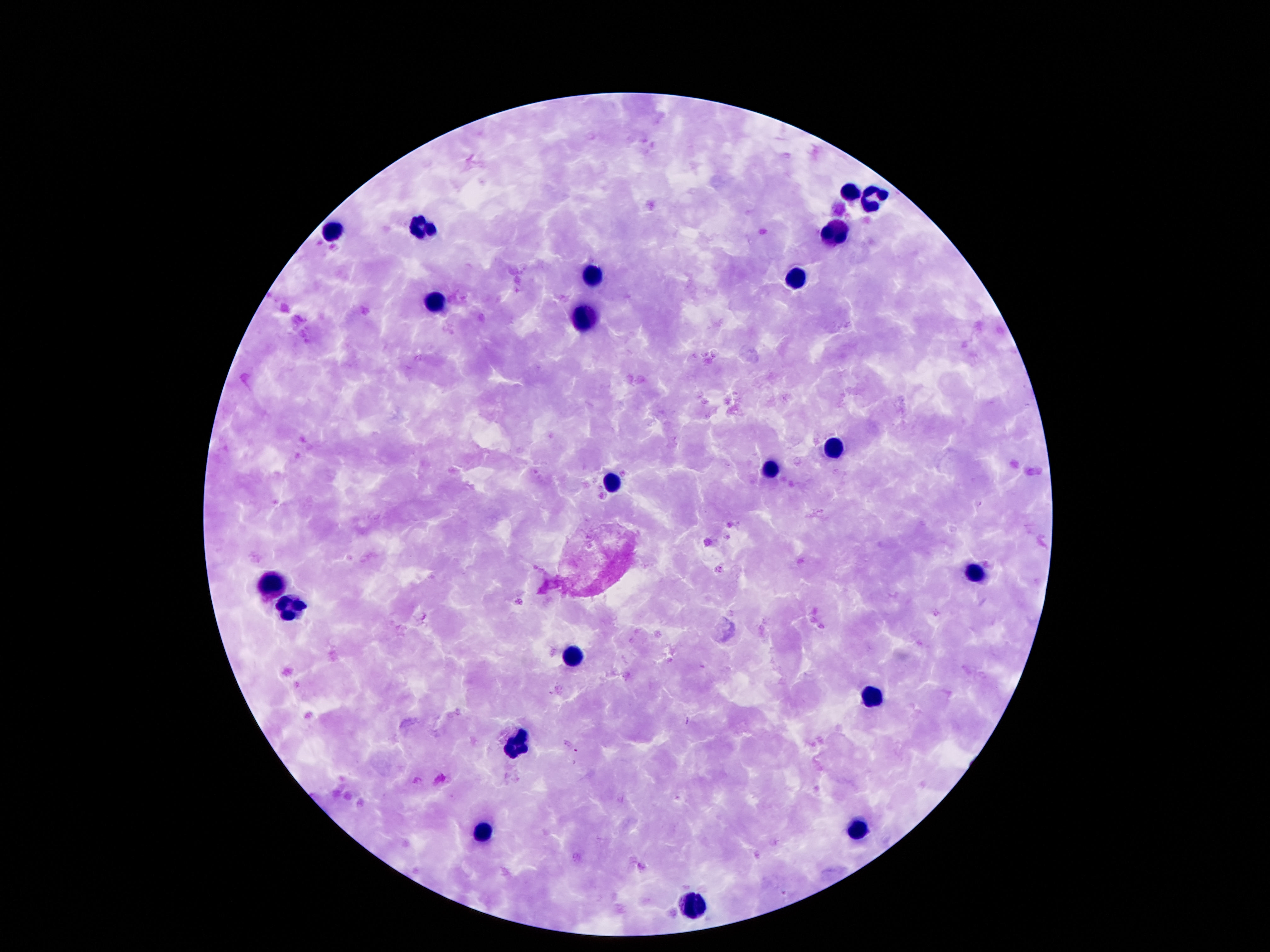

Approximate centers as {x, y} in pixels.
Summary:
  - Leukocyte locations: {850, 192}, {875, 200}, {424, 228}, {334, 232}, {836, 232}, {594, 278}, {795, 280}, {434, 304}, {584, 319}, {834, 447}, {768, 470}, {611, 484}, {977, 575}, {272, 584}, {289, 610}, {570, 659}, {873, 695}, {516, 747}, {858, 831}, {481, 833}, {692, 907}
  - Stain: Giemsa
  - Patient malaria status: uninfected
  - Field of view: single
  - Capture: smartphone camera through the microscope eyepiece
  - Preparation: thick peripheral-blood smear
  - Magnification: 100x
  - Image size: 1270×952 pixels